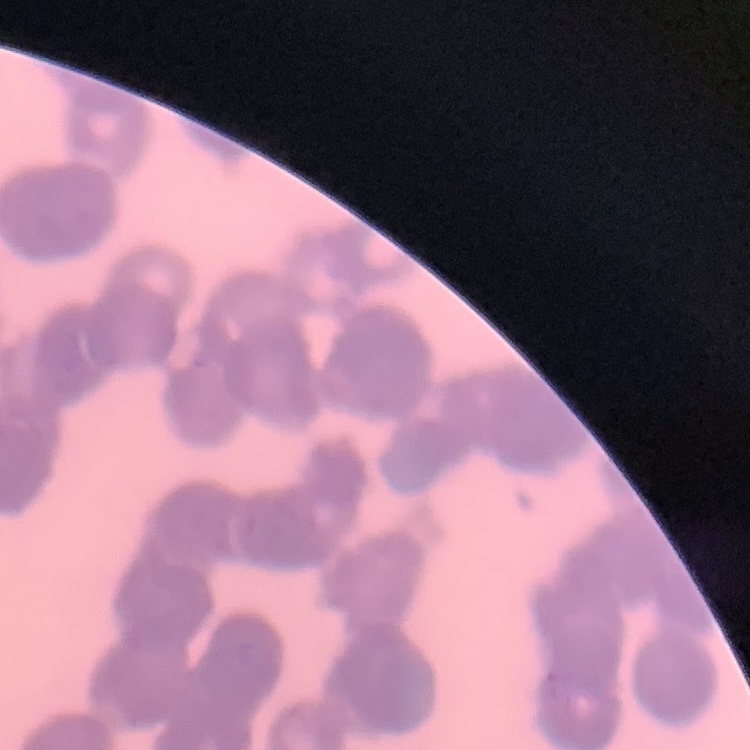

red_blood_cell_morphology: rouleaux formation
image_type: one tile cut from a larger photomicrograph
preparation: thin blood smear
stain: Field's or Giemsa